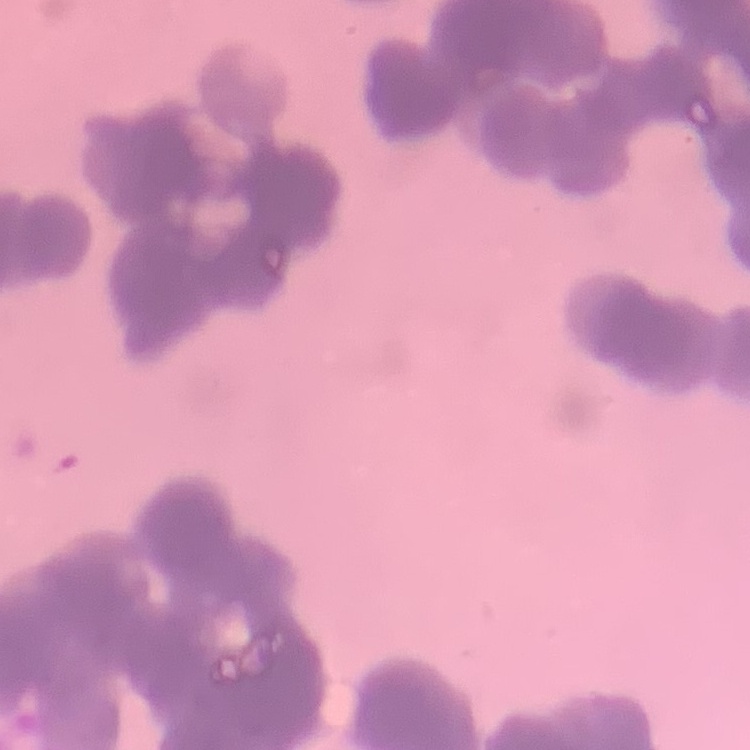

erythrocyte morphology = rouleaux formation
preparation = thin blood film
image type = square crop of a larger photomicrograph
stain = Field's or Giemsa